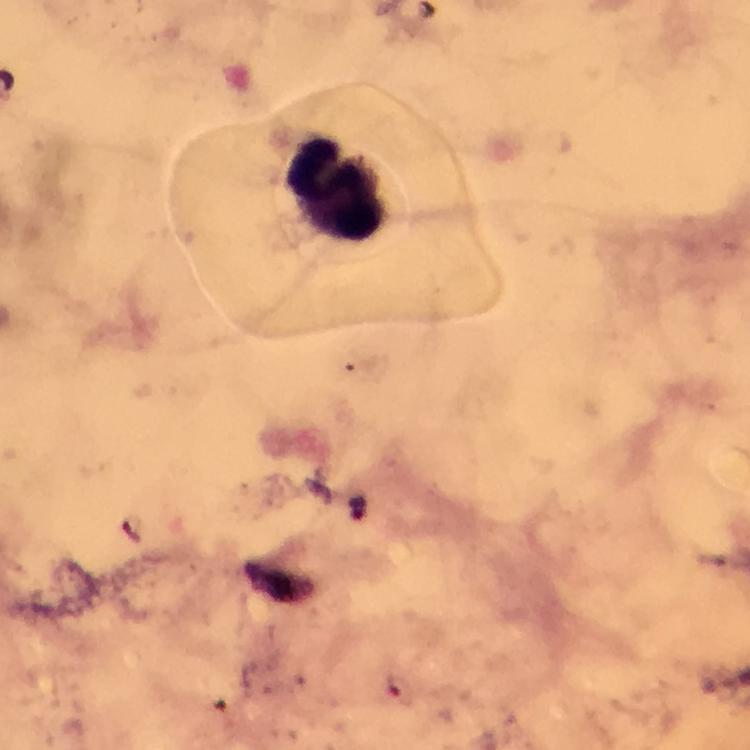
Approximate centers as {x, y} in pixels.
Summary:
  - Leukocyte locations: {339, 187}
  - Plasmodium parasite locations: {359, 506}
  - Cropped from: a single field of view
  - Context: from a malaria diagnostic workup
  - Stain: Giemsa
  - Immersion oil: applied
  - Image size: 750×750 pixels
  - Capture: smartphone camera through the microscope
  - Preparation: thick smear
  - Magnification: 100x